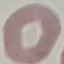
result: no malaria parasites detected
capture: smartphone camera at the microscope eyepiece
stain: Giemsa
image_type: cell patch, automatically extracted from a larger field of view and resized to 64 × 64 pixels
preparation: thin blood film